Assess the morphology of the red blood cells.
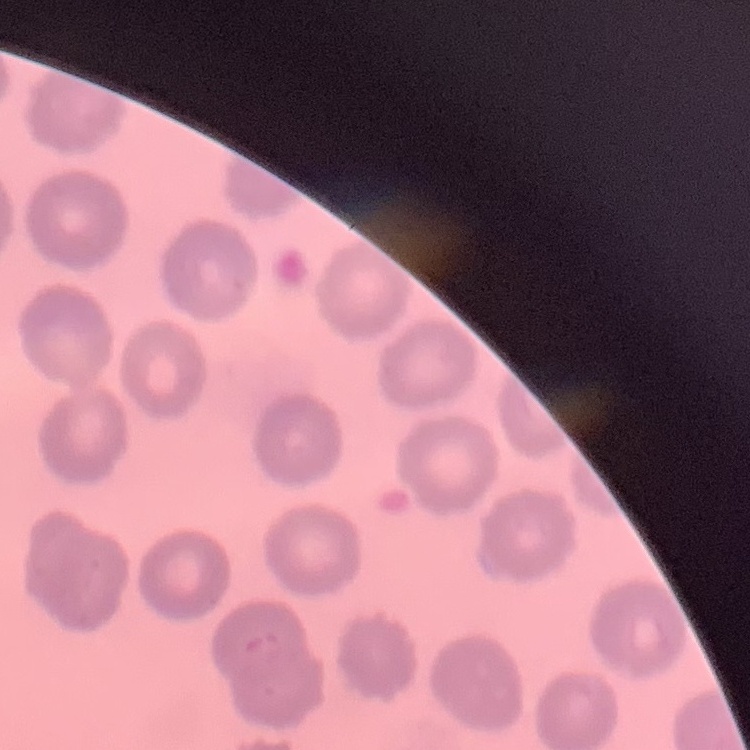

No rouleaux formation.

{
  "stain": "Field's or Giemsa",
  "image_type": "square crop of a larger photomicrograph",
  "preparation": "thin blood smear"
}